Report the malaria status of this cell.
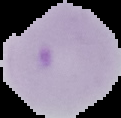
It is parasitized.

Summary:
  - Image type: segmented cell region on a black background
  - Preparation: thin blood film
  - Image size: 121×118 pixels